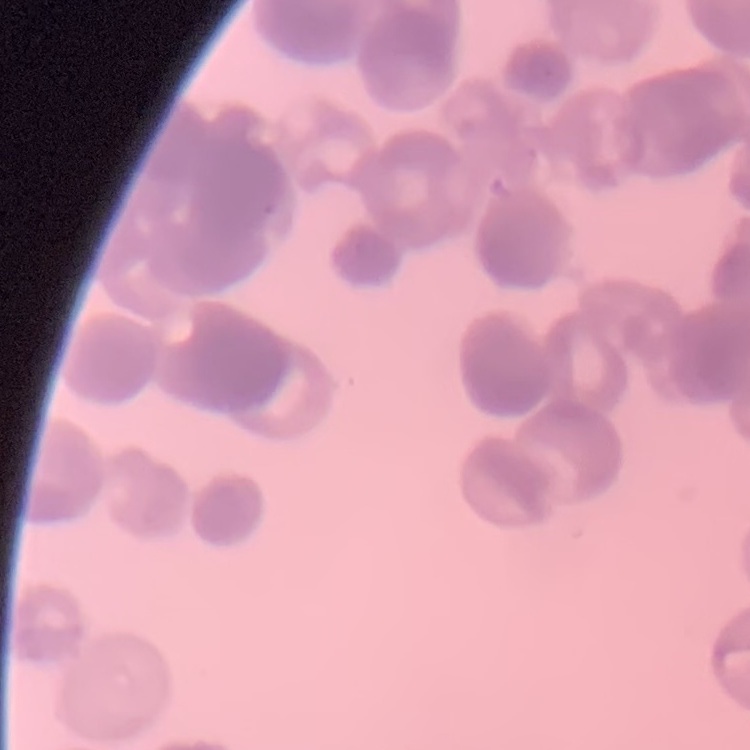
{
  "red_blood_cell_morphology": "rouleaux formation",
  "stain": "Field's or Giemsa",
  "preparation": "thin blood film",
  "image_type": "square crop of a larger photomicrograph"
}